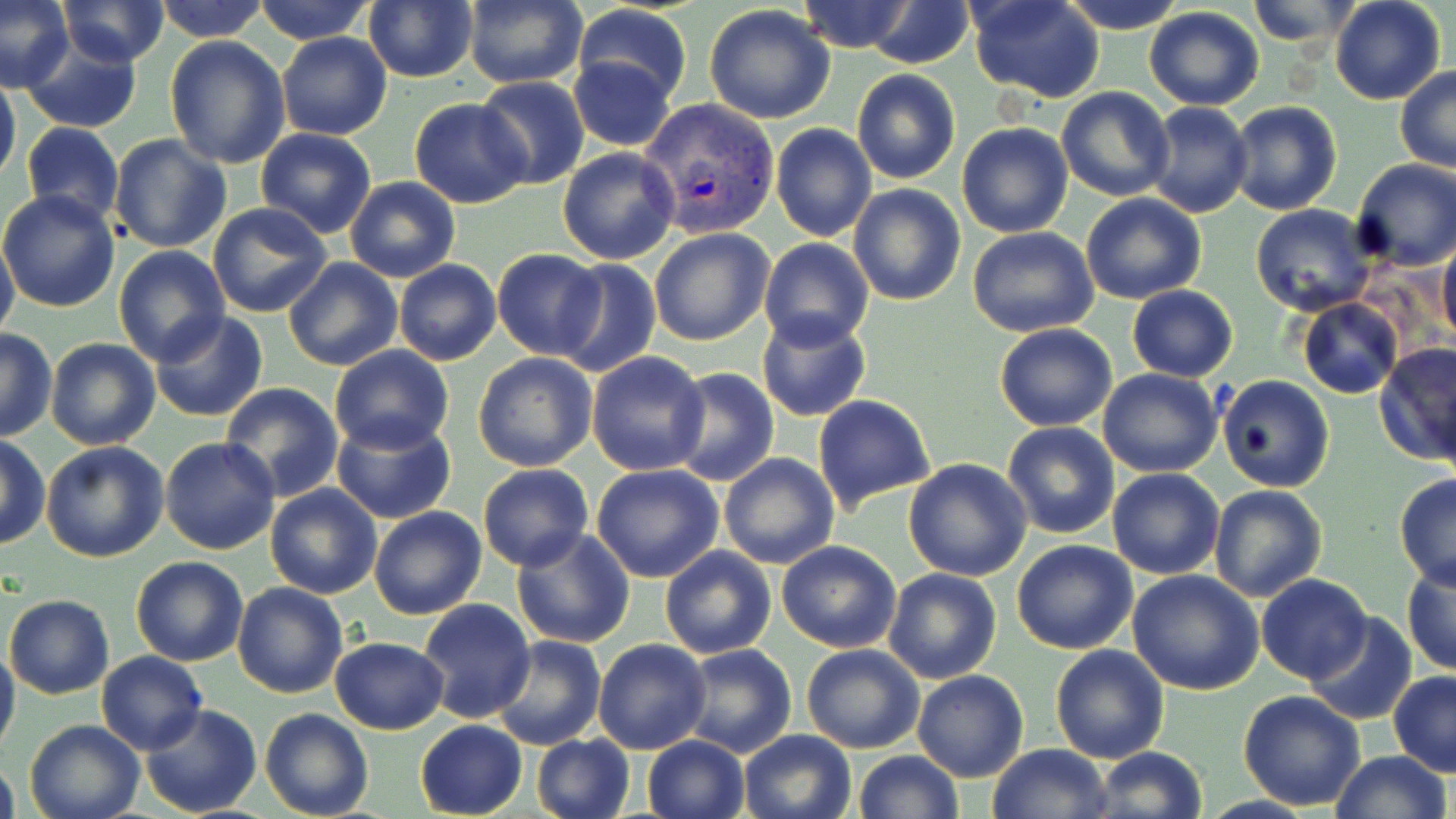

Approximate bounding boxes as [x1, y1, x2, y2] in pixels. Plasmodium vivax-infected red blood cell locations: [641, 96, 782, 239]. Uninfected red blood cell locations: [0, 0, 71, 90], [57, 0, 171, 66], [153, 0, 270, 41], [793, 0, 920, 54], [859, 0, 978, 69], [966, 0, 1105, 103], [1055, 0, 1189, 32], [1245, 0, 1359, 49], [1330, 0, 1447, 105], [249, 1, 380, 45], [460, 1, 589, 89], [362, 2, 479, 83], [571, 3, 691, 108], [704, 5, 836, 124], [1143, 7, 1266, 110], [276, 31, 393, 141], [19, 34, 144, 134], [165, 36, 291, 171], [566, 49, 681, 152], [1395, 65, 1456, 172], [851, 68, 962, 184], [0, 75, 20, 192], [475, 75, 588, 191], [1057, 86, 1174, 201], [409, 97, 531, 209], [1228, 101, 1344, 216], [1144, 102, 1254, 218], [22, 121, 124, 226], [956, 121, 1074, 238], [770, 123, 876, 242], [256, 127, 377, 239], [109, 133, 233, 255], [557, 146, 681, 265], [1350, 158, 1456, 271], [344, 177, 459, 283], [847, 183, 966, 305], [0, 189, 121, 313], [1080, 193, 1206, 305], [206, 201, 333, 319], [1249, 203, 1376, 316], [968, 228, 1098, 337], [650, 229, 775, 346], [0, 232, 19, 347], [1437, 236, 1456, 347], [757, 238, 873, 350], [113, 246, 229, 365], [492, 249, 606, 360], [281, 258, 402, 371], [552, 258, 661, 380], [393, 259, 501, 366], [1126, 285, 1238, 382], [1296, 297, 1404, 400], [150, 311, 269, 423], [755, 311, 871, 422], [994, 323, 1119, 432], [1, 330, 56, 440], [46, 339, 161, 451], [183, 342, 313, 481], [1375, 342, 1456, 465], [328, 344, 455, 454], [587, 351, 711, 476], [472, 352, 598, 471], [667, 367, 779, 486], [1096, 368, 1222, 478], [1217, 375, 1334, 493], [220, 382, 344, 500], [812, 394, 938, 514], [330, 414, 456, 525], [1002, 421, 1120, 539], [0, 436, 48, 550], [159, 437, 281, 556], [40, 441, 170, 562], [719, 452, 839, 570], [903, 457, 1032, 581], [477, 464, 592, 571], [591, 464, 725, 583], [1106, 467, 1225, 580], [1394, 474, 1456, 590], [1209, 484, 1327, 602], [265, 485, 382, 599], [369, 505, 488, 620], [511, 527, 636, 648], [1012, 539, 1138, 654], [776, 540, 903, 652], [659, 545, 778, 659], [132, 556, 248, 666], [1402, 563, 1456, 676], [881, 567, 1002, 684], [1127, 570, 1264, 696], [1257, 575, 1372, 684], [231, 583, 347, 699], [4, 593, 114, 699], [417, 598, 535, 723], [1303, 613, 1418, 726], [491, 636, 607, 752], [330, 637, 449, 734], [591, 639, 710, 755], [0, 643, 20, 758], [678, 643, 797, 757], [800, 643, 925, 753], [1050, 643, 1169, 764], [97, 651, 207, 756], [912, 669, 1028, 782], [1389, 671, 1456, 776], [1237, 690, 1366, 810], [140, 704, 264, 819], [260, 707, 375, 819], [23, 718, 146, 819], [413, 719, 526, 819], [737, 730, 856, 819], [530, 734, 635, 819], [641, 735, 750, 819], [988, 744, 1112, 819], [1092, 747, 1208, 819], [852, 750, 964, 819], [1330, 750, 1452, 819], [0, 757, 19, 819]. Slide-level diagnosis: Plasmodium vivax. One field of a larger specimen. Image is 1456×819 pixels. Thin blood film. Optical microscopy. 1000x magnification. May-Grünwald-Giemsa-stained preparation.